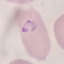

Result: malaria parasites identified. Cell patch, automatically extracted from a larger field of view and resized to 64 × 64 pixels. Giemsa stain. Acquired by smartphone through the microscope eyepiece. Thin blood film.